Name the blood parasite species.
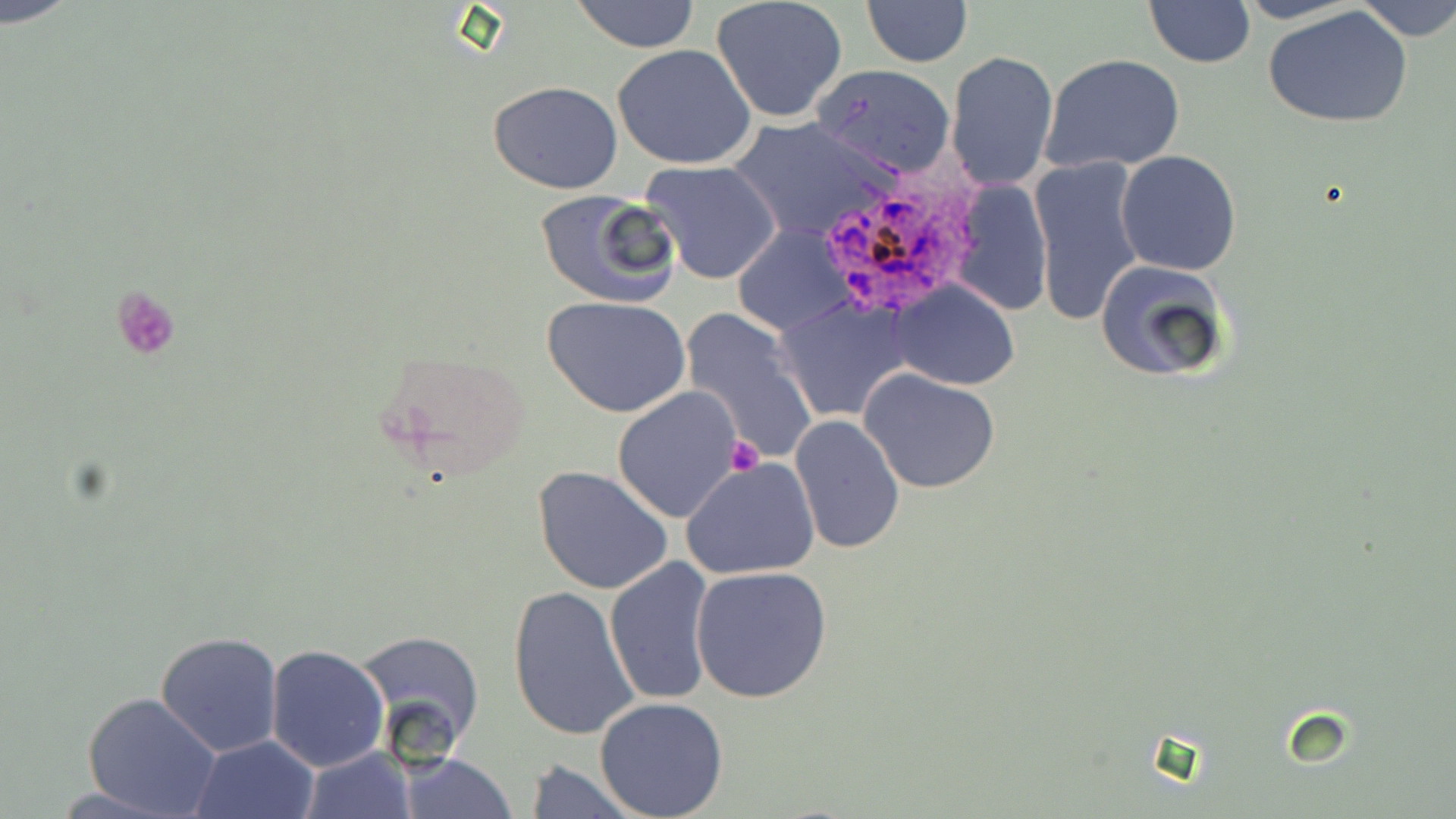
Plasmodium ovale.

Summary:
  - Coordinate format: approximate bounding boxes as named x1/y1/x2/y2 corners in pixels
  - Uninfected red blood cell locations: (x1=2, y1=0, x2=79, y2=27), (x1=570, y1=0, x2=701, y2=51), (x1=1232, y1=0, x2=1367, y2=24), (x1=1347, y1=0, x2=1455, y2=41), (x1=711, y1=1, x2=849, y2=124), (x1=861, y1=1, x2=973, y2=68), (x1=1143, y1=1, x2=1255, y2=69), (x1=1265, y1=6, x2=1415, y2=131), (x1=612, y1=45, x2=759, y2=170), (x1=946, y1=50, x2=1059, y2=190), (x1=1039, y1=53, x2=1186, y2=175), (x1=815, y1=65, x2=956, y2=177), (x1=488, y1=81, x2=623, y2=195), (x1=730, y1=116, x2=896, y2=241), (x1=1115, y1=151, x2=1243, y2=276), (x1=1029, y1=156, x2=1147, y2=328), (x1=640, y1=160, x2=783, y2=284), (x1=947, y1=178, x2=1053, y2=318), (x1=535, y1=189, x2=683, y2=309), (x1=732, y1=226, x2=850, y2=337), (x1=1094, y1=257, x2=1235, y2=385), (x1=889, y1=281, x2=1020, y2=390), (x1=543, y1=297, x2=691, y2=418), (x1=772, y1=298, x2=913, y2=420), (x1=680, y1=308, x2=817, y2=462), (x1=859, y1=368, x2=1002, y2=494), (x1=613, y1=387, x2=745, y2=523), (x1=789, y1=415, x2=905, y2=557), (x1=682, y1=457, x2=820, y2=580), (x1=533, y1=465, x2=673, y2=596), (x1=604, y1=556, x2=718, y2=707), (x1=690, y1=564, x2=833, y2=705), (x1=507, y1=587, x2=641, y2=743), (x1=154, y1=632, x2=284, y2=758), (x1=351, y1=632, x2=486, y2=758), (x1=264, y1=644, x2=390, y2=772), (x1=81, y1=692, x2=222, y2=819), (x1=594, y1=697, x2=729, y2=819), (x1=189, y1=733, x2=321, y2=819), (x1=297, y1=746, x2=414, y2=818), (x1=396, y1=751, x2=518, y2=818), (x1=521, y1=760, x2=643, y2=818)
  - Plasmodium ovale-infected red blood cell locations: (x1=806, y1=173, x2=985, y2=323)
  - Platelet locations: (x1=111, y1=287, x2=181, y2=360), (x1=724, y1=437, x2=761, y2=475)
  - Field of view: one of a larger specimen
  - Magnification: 1000x
  - Preparation: thin blood smear
  - Modality: light microscopy
  - Image size: 1456×819 pixels
  - Stain: May-Grünwald-Giemsa